Comment on the morphology of the erythrocytes.
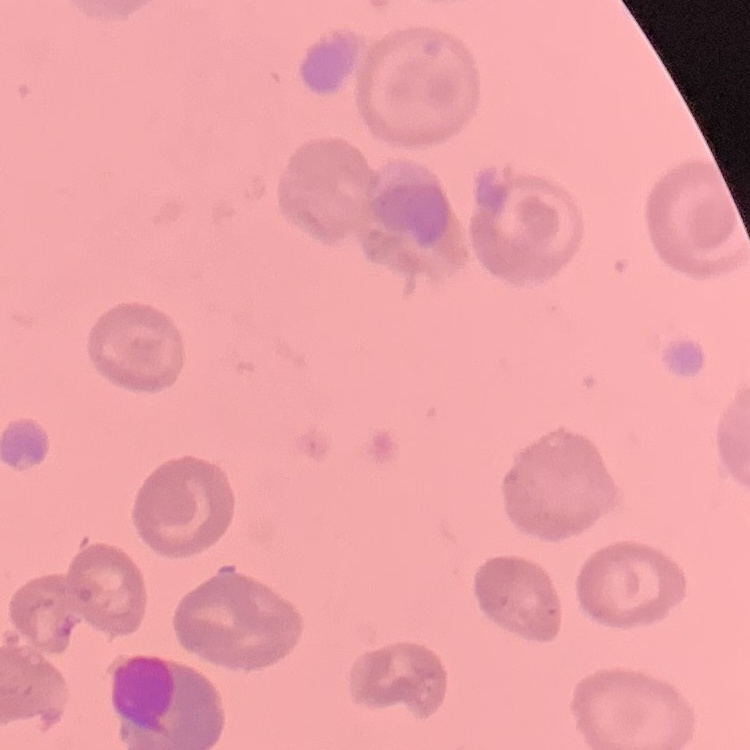
They show no rouleaux formation.

Summary:
  - Image type: one tile cut from a larger photomicrograph
  - Stain: Field's or Giemsa
  - Preparation: thin blood film